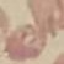

malaria status = uninfected
preparation = thin blood smear
image type = cell patch, automatically extracted from a larger field of view and resized to 64 × 64 pixels
capture = smartphone through the microscope eyepiece
stain = Giemsa